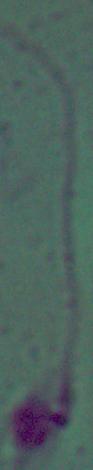

modality = photomicrograph
magnification = 1000x
identification = Leishmania